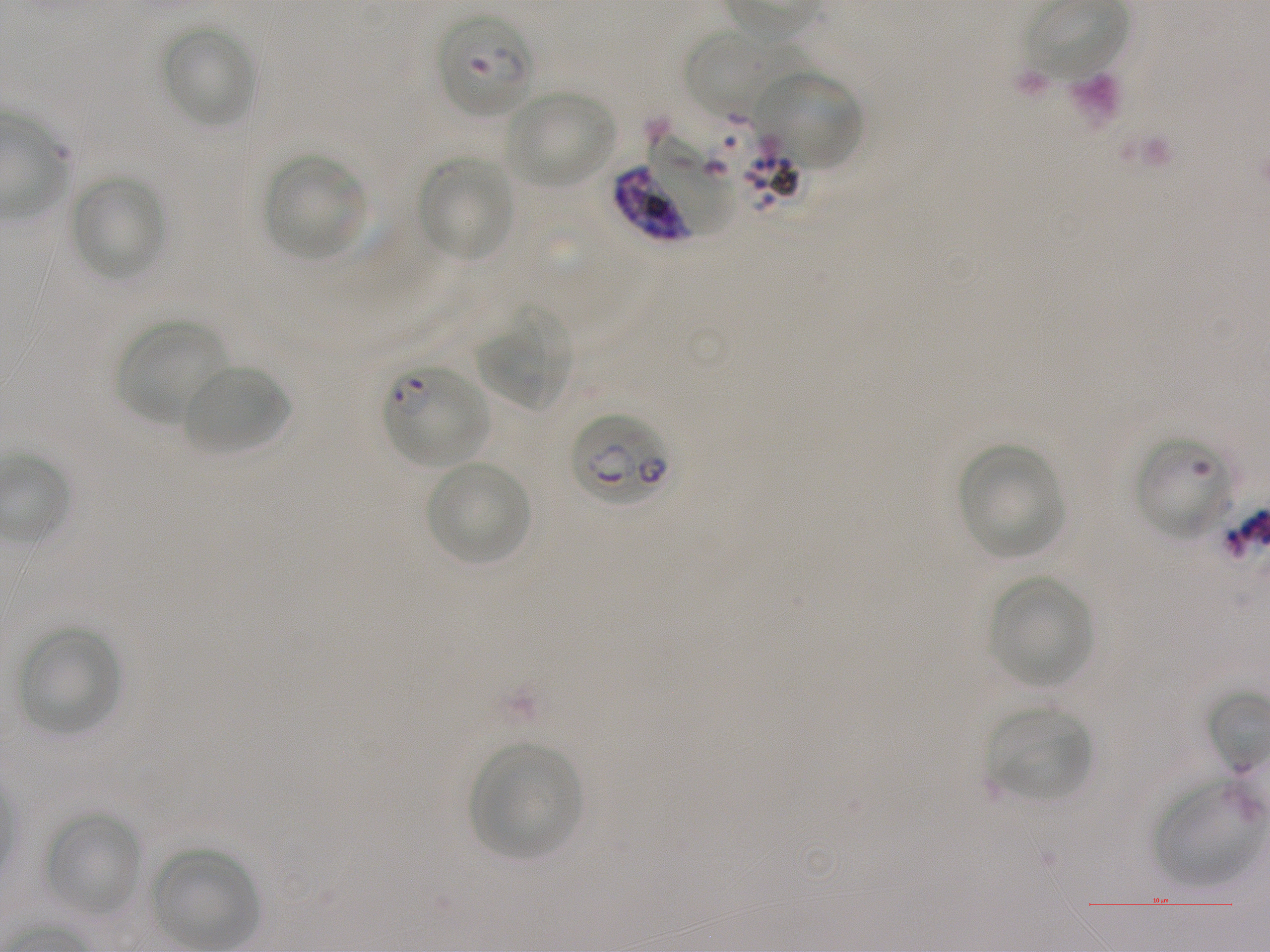 Approximate bounding boxes as {x1, y1, x2, y2} in pixels. Not every red blood cell is marked. A life-cycle stage — or a range of stages, where the recorded stages span more than one — follows each staged infected red blood cell. Locations of uninfected red blood cells: {161, 24, 255, 129}, {681, 27, 811, 118}, {758, 70, 863, 173}, {504, 89, 616, 189}, {264, 154, 367, 260}, {418, 155, 515, 261}, {69, 175, 166, 281}, {478, 312, 571, 410}, {118, 318, 230, 426}, {183, 363, 289, 457}, {958, 444, 1065, 559}, {425, 460, 531, 565}, {987, 576, 1094, 689}, {17, 625, 121, 735}, {986, 705, 1093, 801}, {468, 742, 580, 859}, {1153, 773, 1263, 887}, {45, 811, 142, 916}, {150, 846, 260, 948}. Locations of red blood cells of indeterminate infection status: {1136, 435, 1236, 539}. Locations of infected red blood cells: {437, 12, 535, 119} early ring to early trophozoite; {616, 157, 723, 240} schizont; {384, 366, 490, 469} ring; {571, 411, 672, 506}. Life-cycle stages observed: ring, schizont. 100x objective under oil immersion, numerical aperture 1.25. Giemsa stain. Thin blood film. P. falciparum strain NF54 maintained in static in-vitro culture. Blood group of the donor: A+. Image is 1270×952 pixels. One field from this slide.